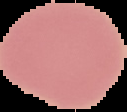
image size = 127×112 pixels
image type = segmented cell region on a black background
preparation = thin blood film
malaria status = uninfected